Identify the cell.
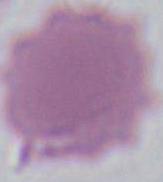

This is an erythrocyte.

modality: photomicrograph
magnification: 1000x